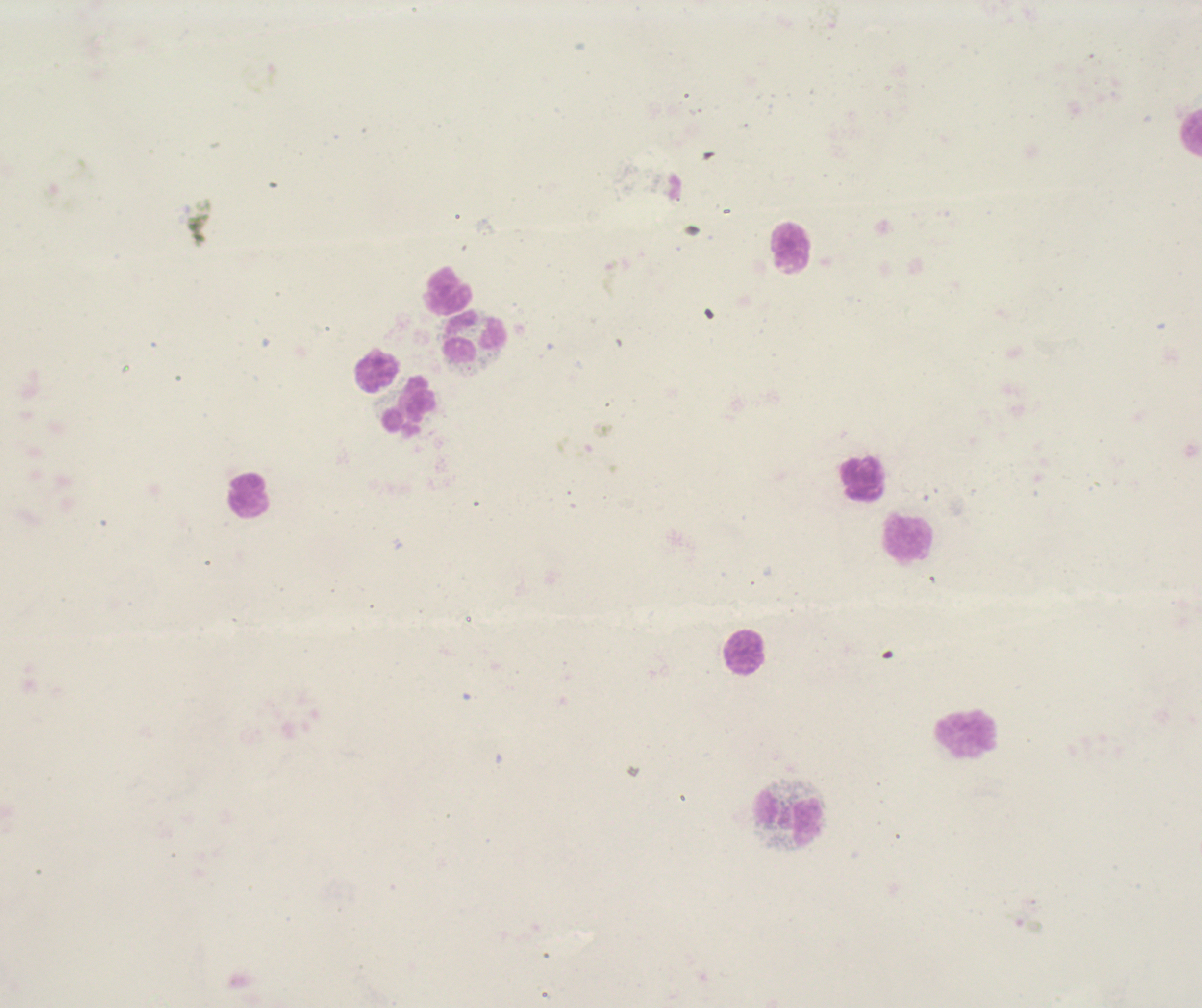
Approximate object centers, in pixels from the top-left corner.
Summary:
  - Leukocyte locations: (x=1191, y=132), (x=791, y=249), (x=448, y=290), (x=475, y=334), (x=376, y=370), (x=410, y=405), (x=863, y=479), (x=248, y=496), (x=909, y=539), (x=745, y=653), (x=965, y=733), (x=789, y=820)
  - Gametocyte locations: (x=610, y=276), (x=587, y=455), (x=1024, y=924)
  - Magnification: 100x
  - Context: previously used in an actual diagnosis
  - Field of view: single
  - Background quality: unsatisfactory
  - Stain: Romanowsky
  - Result: malaria parasites detected
  - Coloration quality: bad
  - Preparation: thick smear of blood
  - Image size: 1202×1008 pixels